Name the parasite shown.
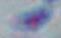
This is Toxoplasma gondii.

modality = photomicrograph
magnification = 1000x